Locate every white blood cell.
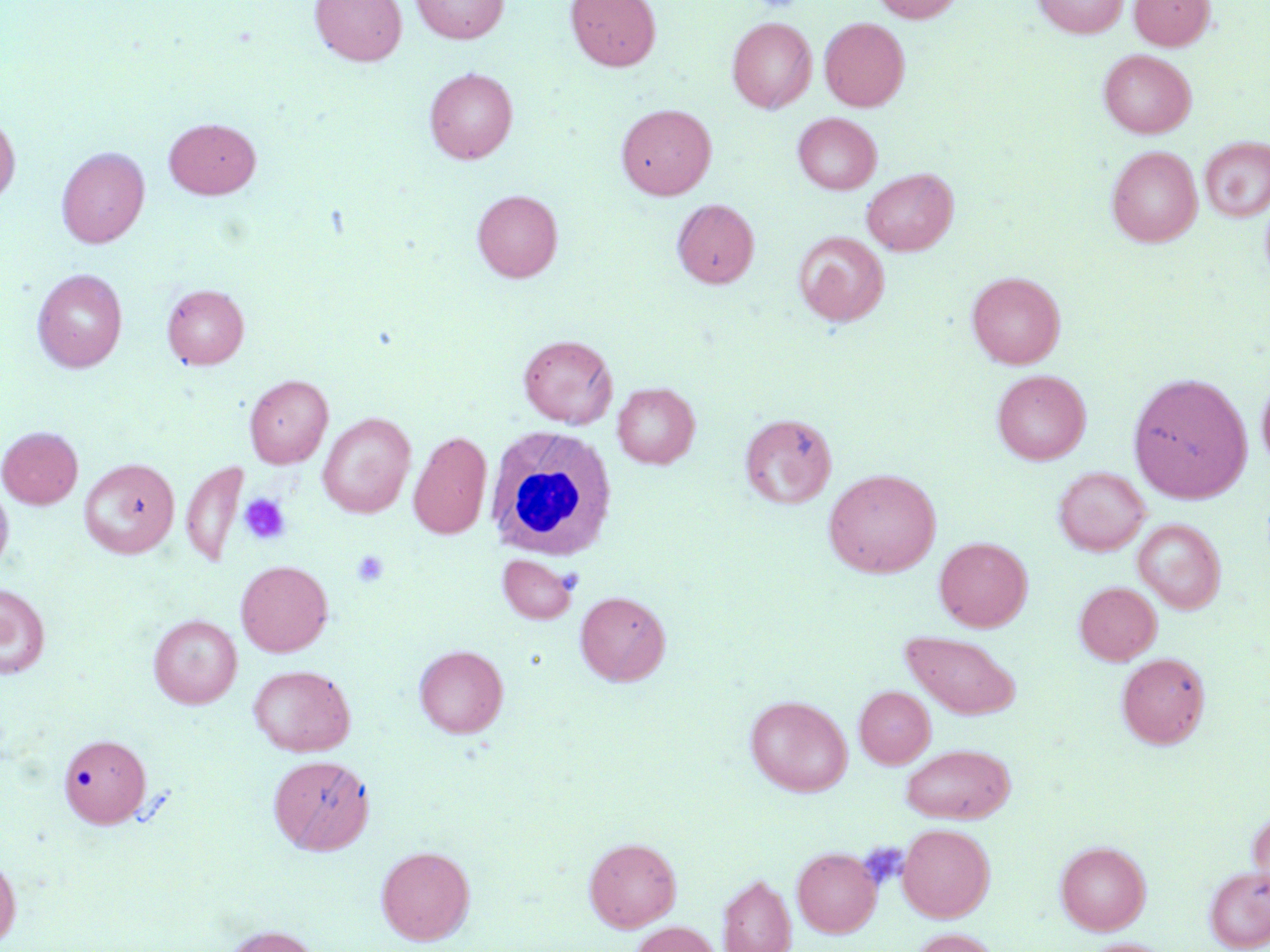
Approximate bounding boxes as (x1,y1)-(x2,y2) corner pairs in pixels.
White blood cells: (486,425)-(618,561).

Summary:
  - Platelet locations: (238,492)-(292,545), (351,549)-(390,587), (861,844)-(908,891)
  - Uninfected red blood cell locations: (310,0)-(407,65), (411,0)-(508,43), (565,0)-(661,71), (871,0)-(963,23), (1033,0)-(1127,38), (1129,0)-(1214,50), (726,17)-(816,113), (819,17)-(910,111), (1099,49)-(1196,138), (424,68)-(518,164), (616,103)-(716,199), (793,112)-(881,194), (0,113)-(20,206), (164,117)-(261,198), (1200,136)-(1270,222), (1106,145)-(1202,246), (56,146)-(150,248), (861,168)-(958,256), (472,190)-(563,282), (672,199)-(760,288), (793,231)-(890,326), (32,268)-(127,372), (966,271)-(1065,368), (162,284)-(249,368), (518,334)-(617,428), (992,369)-(1091,465), (1128,371)-(1252,503), (1257,373)-(1270,472), (244,374)-(332,468), (613,382)-(700,468), (317,412)-(416,518), (740,412)-(837,509), (0,426)-(83,508), (409,431)-(492,540), (79,458)-(179,558), (181,460)-(248,568), (1054,466)-(1150,556), (823,468)-(942,578), (0,482)-(14,574), (1133,518)-(1225,614), (934,536)-(1032,631), (497,554)-(578,624), (235,560)-(333,657), (1074,581)-(1162,665), (0,583)-(50,679), (575,590)-(670,686), (148,615)-(241,708), (901,631)-(1021,719), (414,645)-(509,738), (1116,652)-(1210,749), (248,664)-(355,756), (855,686)-(935,768), (745,695)-(852,797), (58,732)-(151,828), (900,743)-(1015,823), (268,754)-(374,855), (1248,803)-(1270,903), (897,823)-(995,922), (583,837)-(681,932), (1055,840)-(1151,935), (375,845)-(475,945), (792,847)-(881,937), (0,853)-(21,947), (1204,865)-(1270,952), (718,874)-(796,952), (629,921)-(721,952), (223,924)-(324,952), (907,928)-(1001,952), (1081,939)-(1172,952)
  - Slide-level diagnosis: negative for blood parasites
  - Preparation: thin blood film
  - Magnification: 1000x
  - Image size: 1270×952 pixels
  - Modality: light microscopy
  - Stain: May-Grünwald-Giemsa
  - Field of view: one of a larger specimen